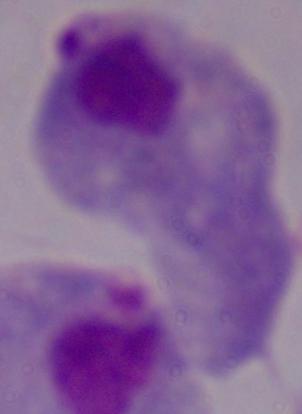

Photomicrograph. A trichomonad is seen. Captured at 1000x magnification.